Classify this cell by malaria status.
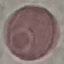

Uninfected.

Thin blood smear. Giemsa stain. Cell patch, automatically extracted from a larger field of view and resized to 64 × 64 pixels. Acquired by smartphone through the microscope eyepiece.